Assess this cell for malaria.
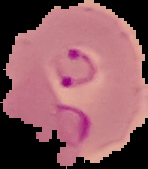

It is parasitized.

preparation = thin blood film
image type = segmented cell region on a black background
image size = 148×169 pixels